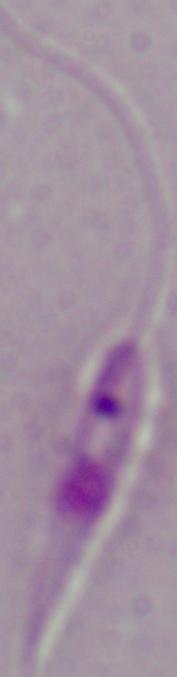

Summary:
  - Magnification: 1000x
  - Identification: Leishmania
  - Modality: micrograph